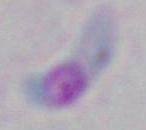

modality = micrograph
identification = Toxoplasma gondii
magnification = 1000x